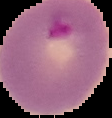
image type = cell region segmented out of the field of view; surrounding area masked to black
preparation = thin blood smear
result = Plasmodium parasites detected
image size = 112×118 pixels